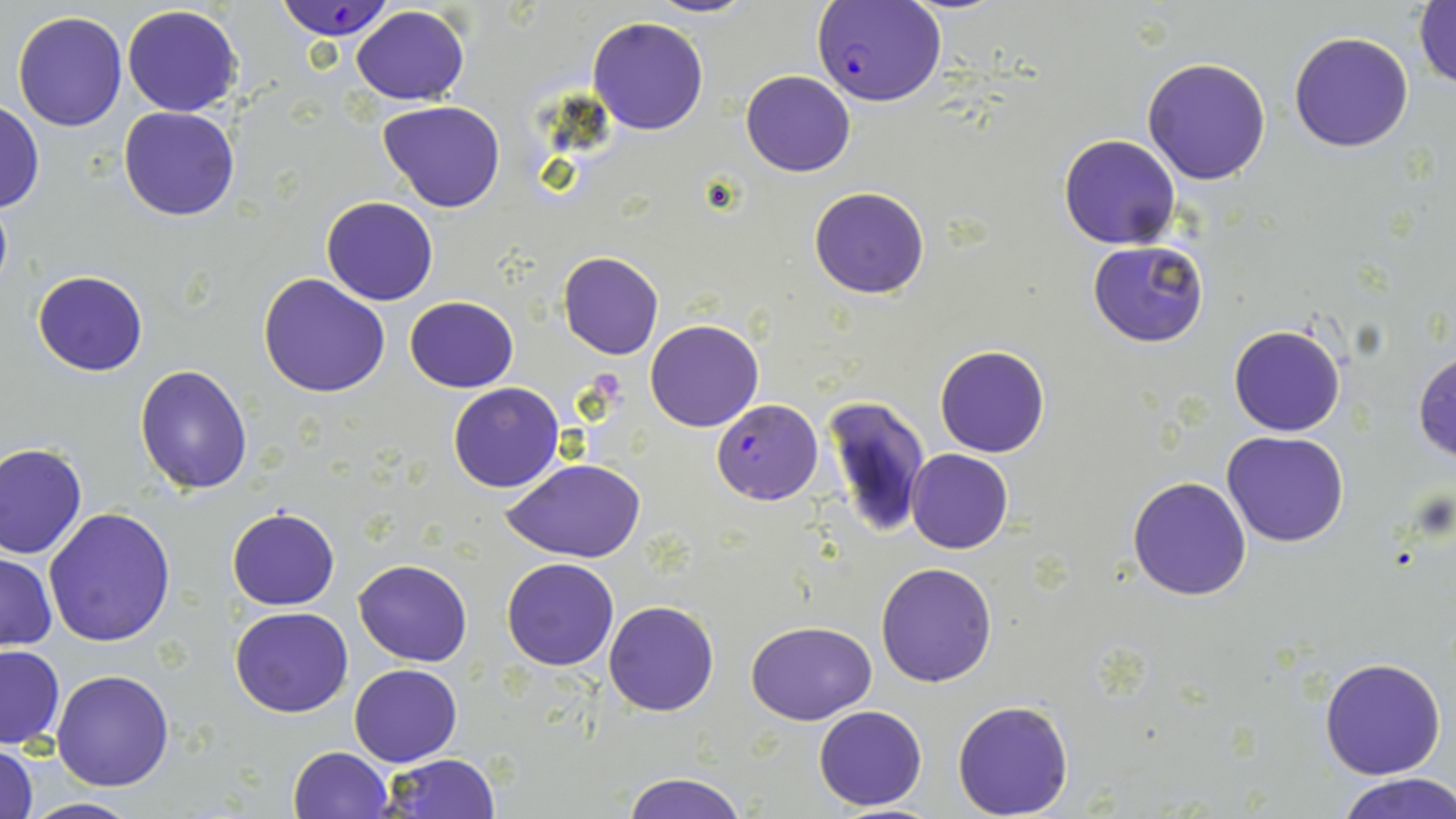

Summary:
  - Coordinate format: approximate bounding boxes as named x1/y1/x2/y2 corners in pixels
  - Uninfected red blood cell locations: (x1=647, y1=0, x2=755, y2=19), (x1=1412, y1=3, x2=1456, y2=90), (x1=122, y1=4, x2=242, y2=117), (x1=349, y1=5, x2=472, y2=106), (x1=11, y1=10, x2=127, y2=131), (x1=586, y1=16, x2=710, y2=136), (x1=1289, y1=30, x2=1414, y2=152), (x1=1141, y1=57, x2=1272, y2=186), (x1=740, y1=69, x2=855, y2=176), (x1=379, y1=98, x2=506, y2=212), (x1=0, y1=101, x2=44, y2=212), (x1=117, y1=106, x2=240, y2=221), (x1=1058, y1=133, x2=1181, y2=249), (x1=809, y1=186, x2=931, y2=299), (x1=322, y1=195, x2=439, y2=304), (x1=1089, y1=240, x2=1210, y2=347), (x1=558, y1=252, x2=665, y2=360), (x1=32, y1=269, x2=149, y2=376), (x1=258, y1=273, x2=391, y2=397), (x1=404, y1=295, x2=519, y2=393), (x1=645, y1=319, x2=763, y2=432), (x1=1229, y1=323, x2=1346, y2=436), (x1=935, y1=344, x2=1050, y2=458), (x1=1413, y1=348, x2=1456, y2=464), (x1=134, y1=365, x2=253, y2=495), (x1=447, y1=383, x2=564, y2=493), (x1=822, y1=393, x2=930, y2=539), (x1=1222, y1=430, x2=1349, y2=547), (x1=1, y1=442, x2=87, y2=560), (x1=906, y1=448, x2=1013, y2=553), (x1=503, y1=459, x2=645, y2=563), (x1=1128, y1=476, x2=1252, y2=601), (x1=226, y1=506, x2=340, y2=612), (x1=43, y1=508, x2=177, y2=648), (x1=1, y1=553, x2=57, y2=650), (x1=501, y1=557, x2=619, y2=670), (x1=353, y1=558, x2=473, y2=666), (x1=877, y1=562, x2=997, y2=686), (x1=604, y1=600, x2=719, y2=716), (x1=229, y1=607, x2=353, y2=718), (x1=745, y1=619, x2=876, y2=725), (x1=0, y1=644, x2=63, y2=748), (x1=1318, y1=657, x2=1446, y2=779), (x1=349, y1=664, x2=462, y2=766), (x1=51, y1=669, x2=176, y2=791), (x1=952, y1=700, x2=1074, y2=818), (x1=813, y1=705, x2=927, y2=810), (x1=1, y1=743, x2=38, y2=819), (x1=288, y1=745, x2=392, y2=818), (x1=382, y1=753, x2=503, y2=818), (x1=619, y1=771, x2=749, y2=819), (x1=1337, y1=774, x2=1456, y2=819), (x1=18, y1=797, x2=144, y2=818)
  - Plasmodium falciparum-infected red blood cell locations: (x1=274, y1=1, x2=400, y2=43), (x1=811, y1=1, x2=945, y2=109), (x1=712, y1=401, x2=821, y2=504)
  - Slide-level diagnosis: Plasmodium falciparum
  - Preparation: thin blood smear
  - Magnification: 1000x
  - Field of view: single
  - Image size: 1456×819 pixels
  - Modality: light microscopy
  - Stain: May-Grünwald-Giemsa